Assess this cell for malaria.
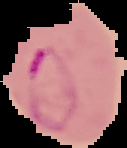

It is parasitized.

The area outside the segmented cell region is set to black. Image is 127×148 pixels. From a thin blood smear.